Give the extent of all uninfected red blood cells.
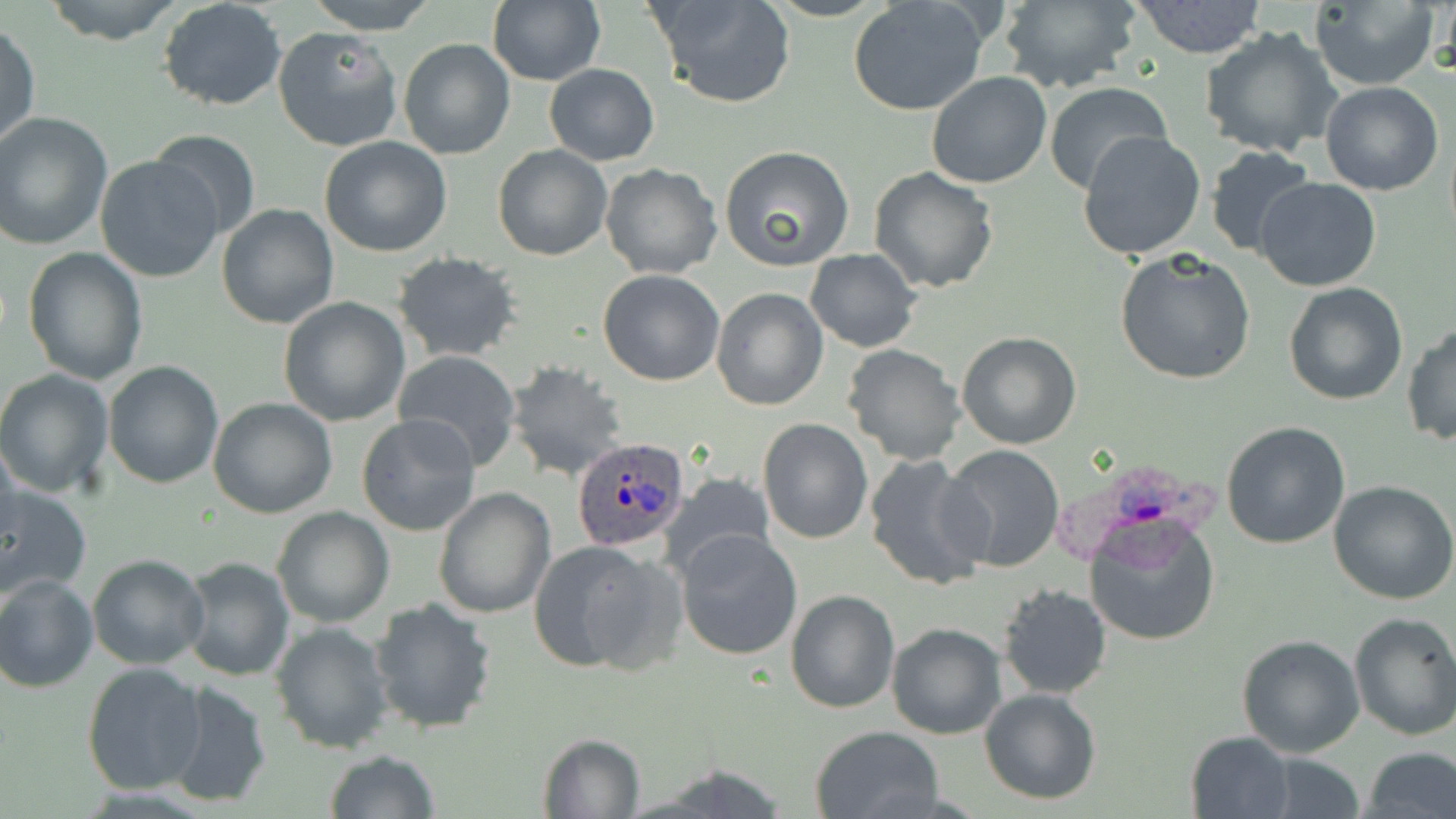

Approximate bounding boxes as (x1, y1, x2, y2) in pixels.
Uninfected red blood cells: (42, 0, 186, 45), (305, 0, 438, 34), (488, 0, 605, 87), (652, 0, 796, 109), (1309, 0, 1440, 90), (158, 1, 288, 112), (847, 1, 991, 115), (998, 1, 1140, 92), (1130, 1, 1267, 58), (1, 20, 40, 154), (272, 27, 402, 151), (1200, 27, 1342, 159), (398, 38, 515, 161), (543, 64, 659, 166), (926, 73, 1052, 189), (1044, 81, 1172, 194), (1320, 82, 1443, 196), (1, 113, 115, 252), (147, 127, 261, 241), (1077, 129, 1207, 261), (319, 136, 453, 258), (492, 145, 612, 261), (719, 145, 854, 270), (1204, 146, 1319, 261), (94, 155, 224, 283), (600, 163, 723, 279), (868, 166, 999, 294), (1254, 176, 1382, 292), (217, 203, 339, 329), (23, 246, 148, 385), (804, 248, 921, 352), (1115, 248, 1257, 386), (391, 252, 523, 362), (597, 269, 726, 387), (1282, 282, 1408, 405), (710, 286, 828, 411), (279, 296, 411, 427), (1403, 322, 1456, 446), (955, 331, 1082, 450), (841, 344, 966, 464), (391, 350, 523, 470), (102, 360, 226, 488), (503, 361, 630, 482), (0, 369, 116, 500), (208, 398, 337, 518), (356, 413, 482, 537), (758, 419, 872, 543), (1221, 421, 1351, 549), (0, 437, 21, 553), (940, 445, 1068, 573), (865, 452, 987, 591), (658, 474, 780, 580), (1329, 481, 1456, 604), (0, 484, 92, 601), (433, 488, 555, 619), (271, 506, 395, 628), (1085, 514, 1221, 647), (675, 528, 804, 661), (528, 538, 680, 674), (86, 553, 210, 670), (179, 556, 295, 681), (0, 574, 99, 692), (997, 583, 1111, 699), (785, 590, 899, 713), (368, 598, 498, 736), (1348, 611, 1456, 740), (270, 620, 394, 755), (886, 622, 1006, 739), (1235, 632, 1365, 758), (80, 662, 205, 796), (165, 680, 273, 809), (979, 688, 1104, 804), (809, 725, 946, 819), (537, 732, 648, 818), (1184, 732, 1294, 819), (1362, 746, 1456, 819), (323, 749, 440, 819), (1252, 753, 1369, 819).

slide_level_diagnosis: Plasmodium ovale
field_of_view: one of a larger specimen
image_size: 1456×819 pixels
magnification: 1000x
modality: optical microscopy
stain: May-Grünwald-Giemsa
plasmodium_ovale_infected_red_blood_cell_locations: 'approximate bounding boxes as (x1, y1, x2, y2) in pixels: (572, 436, 692, 551), (1049, 464, 1222, 576)'
preparation: thin blood film